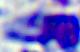
Summary:
  - Magnification: 400x
  - Identification: white blood cell
  - Modality: photomicrograph